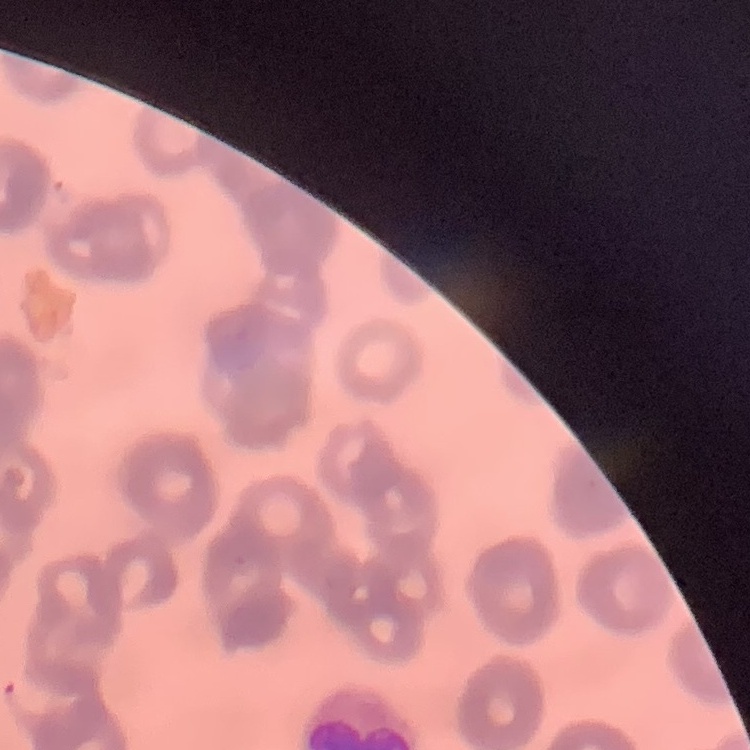
The red blood cells exhibit rouleaux formation. Square crop of a larger photomicrograph. Thin blood smear. Field's or Giemsa stain.